Name the parasite shown.
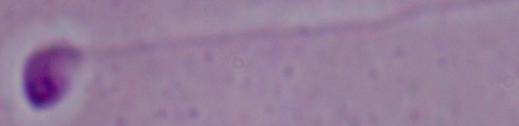
This is Leishmania.

modality: photomicrograph
magnification: 1000x